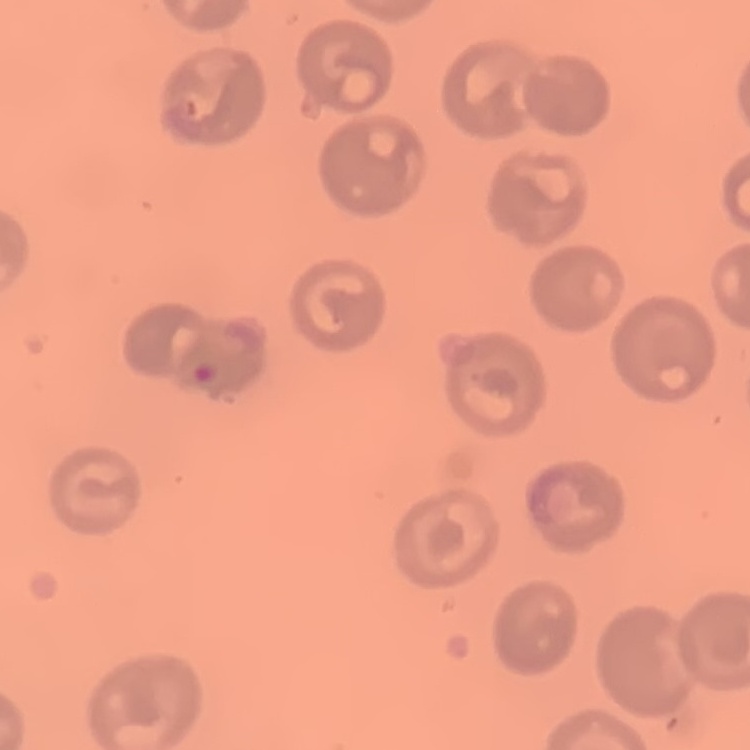 The red blood cells show no rouleaux formation. Thin blood film. Square crop of a larger photomicrograph. Stained with either Field's or Giemsa.